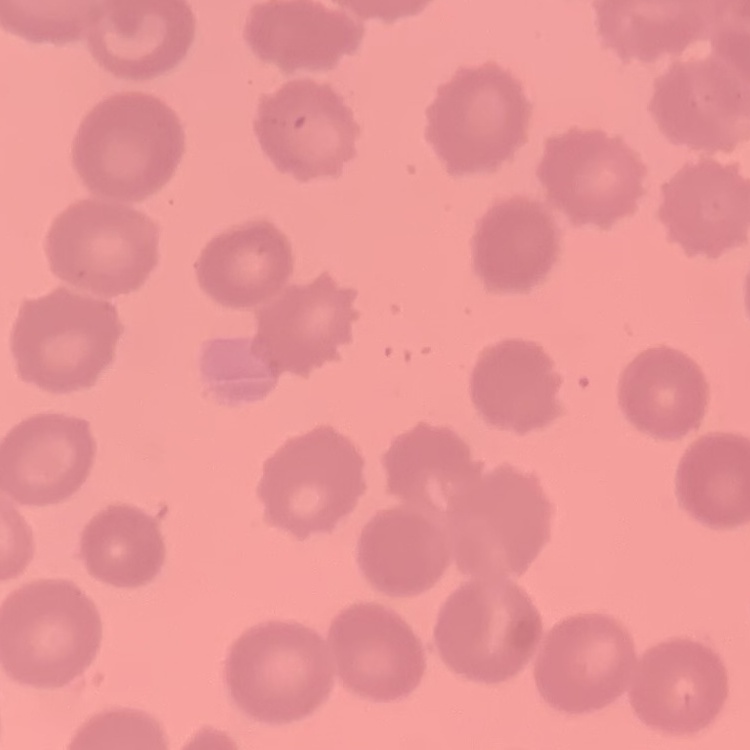
Summary:
  - Red blood cell morphology: no rouleaux formation
  - Preparation: thin blood film
  - Stain: Field's or Giemsa
  - Image type: square crop of a larger photomicrograph